Point out each Plasmodium parasite.
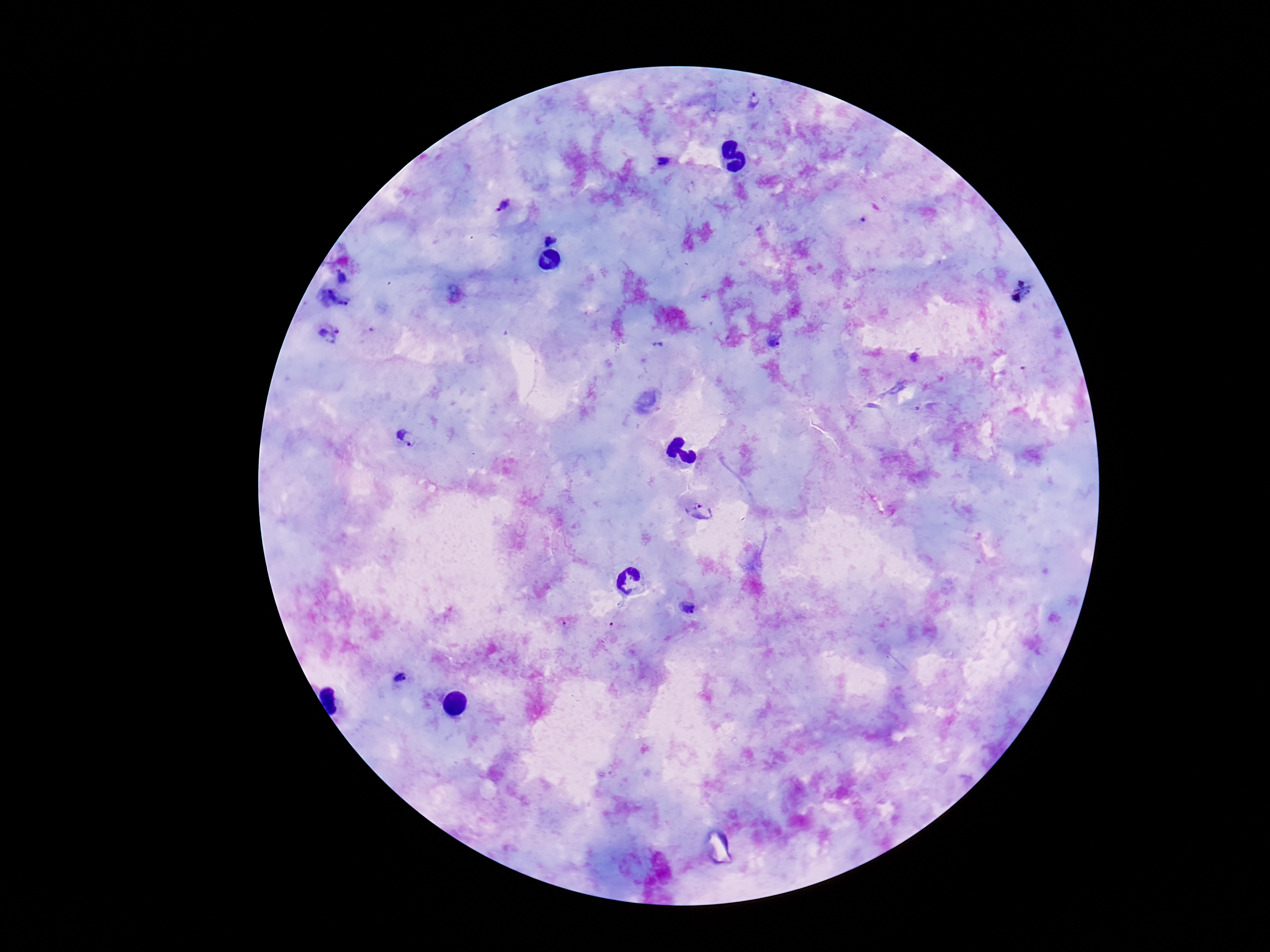
Approximate centers as [x, y] in pixels.
Plasmodium parasites: [754, 101], [663, 162], [503, 206], [550, 240], [344, 276], [333, 300], [329, 334], [774, 337], [406, 437], [701, 511], [687, 608], [401, 678].

Summary:
  - Magnification: 100x
  - Stain: Giemsa
  - Patient malaria status: infected
  - Image size: 1270×952 pixels
  - Field of view: single
  - Capture: smartphone camera through the microscope eyepiece
  - Preparation: thick blood film